Assess this cell for malaria.
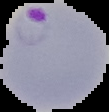
It is parasitized.

Summary:
  - Preparation: thin blood smear
  - Image type: segmented cell region on a black background
  - Image size: 109×112 pixels